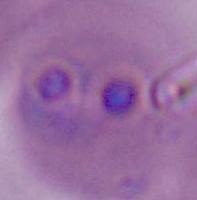

A Plasmodium parasite is seen. 400x or 1000x magnification. Photomicrograph.